Identify the blood parasite species.
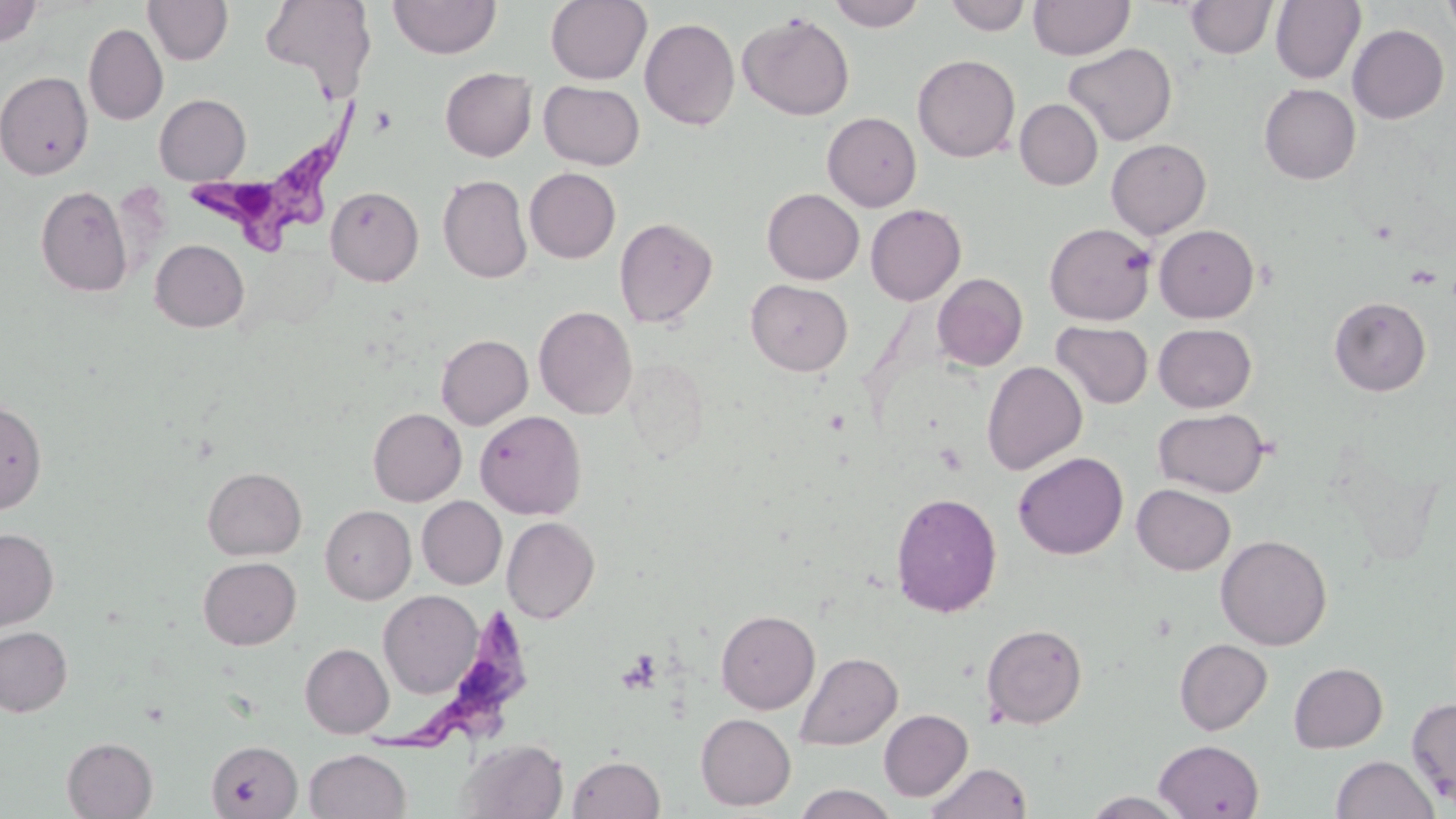
Trypanosoma brucei.

Summary:
  - Coordinate format: approximate bounding boxes as (x1,y1)-(x2,y2) corner pairs in pixels
  - Uninfected red blood cell locations: (259,0)-(377,98), (388,0)-(501,59), (545,0)-(651,85), (826,0)-(927,31), (945,0)-(1031,36), (1028,0)-(1134,60), (1185,0)-(1277,59), (1440,0)-(1456,44), (0,1)-(43,46), (143,1)-(233,65), (1271,1)-(1365,85), (737,12)-(855,121), (639,18)-(739,130), (83,23)-(167,125), (1348,25)-(1449,124), (1064,43)-(1177,146), (912,54)-(1020,162), (440,67)-(536,161), (0,70)-(94,180), (539,80)-(645,170), (1259,83)-(1361,184), (154,94)-(251,185), (1015,99)-(1103,190), (823,112)-(921,211), (1106,139)-(1212,239), (524,168)-(621,263), (437,174)-(532,284), (36,185)-(132,297), (325,187)-(424,286), (762,188)-(864,284), (865,203)-(966,306), (614,217)-(718,329), (1044,222)-(1155,325), (1154,224)-(1259,322), (149,239)-(249,333), (932,273)-(1028,371), (746,280)-(853,375), (1329,296)-(1431,396), (534,304)-(638,420), (1051,321)-(1153,409), (1153,323)-(1257,412), (436,334)-(533,429), (623,358)-(709,462), (981,361)-(1087,475), (0,400)-(47,513), (1153,407)-(1270,497), (368,408)-(466,506), (475,410)-(586,519), (1013,452)-(1128,559), (202,467)-(306,560), (1132,484)-(1236,575), (891,492)-(1002,617), (417,496)-(507,589), (320,505)-(416,604), (502,516)-(599,624), (0,528)-(59,631), (1216,534)-(1332,650), (198,556)-(301,650), (379,589)-(483,699), (716,609)-(820,714), (981,623)-(1087,729), (0,626)-(72,716), (1174,638)-(1272,735), (300,643)-(393,738), (795,651)-(903,751), (1289,662)-(1388,752), (1406,697)-(1456,807), (879,709)-(973,800), (696,713)-(795,810), (62,737)-(157,818), (457,738)-(568,819), (1154,739)-(1264,819), (206,740)-(303,819), (305,749)-(411,819), (567,755)-(665,819), (1331,755)-(1439,819), (925,761)-(1033,819), (795,784)-(899,819), (1082,791)-(1189,818)
  - Trypanosoma brucei locations: (190,82)-(366,255), (370,612)-(527,767)
  - Platelet locations: (1405,264)-(1444,290), (822,409)-(852,434), (935,443)-(967,475)
  - Image size: 1456×819 pixels
  - Field of view: single
  - Stain: May-Grünwald-Giemsa
  - Modality: optical microscopy
  - Preparation: thin blood smear
  - Magnification: 1000x